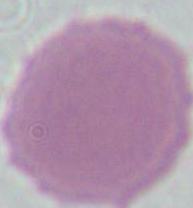

A red blood cell is seen. Photomicrograph. Captured at 1000x magnification.